Assess this cell for malaria.
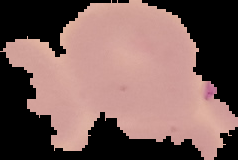
It is uninfected.

image type = segmented cell region with the area outside set to black
image size = 238×160 pixels
preparation = thin blood smear